Point out every Plasmodium parasite and every leukocyte.
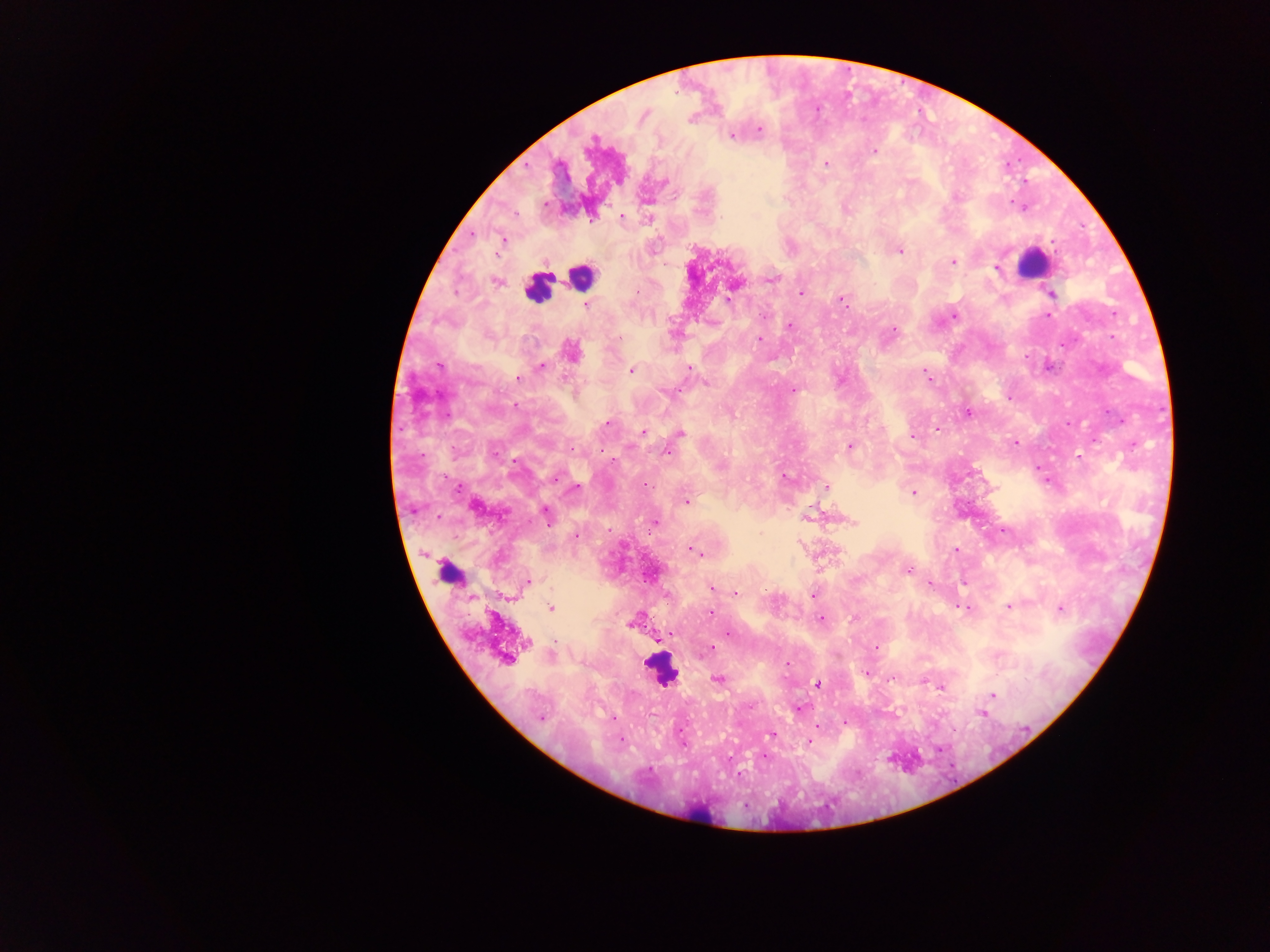

Approximate centers as {x, y} in pixels.
Plasmodium parasites: {643, 116}, {690, 119}, {759, 129}, {732, 136}, {874, 151}, {826, 164}, {664, 183}, {957, 198}, {544, 204}, {622, 216}, {721, 218}, {591, 220}, {501, 239}, {900, 251}, {954, 262}, {996, 268}, {771, 279}, {497, 281}, {637, 292}, {801, 293}, {1051, 294}, {727, 299}, {841, 300}, {586, 306}, {955, 315}, {763, 316}, {1048, 316}, {790, 326}, {893, 329}, {760, 339}, {570, 350}, {439, 366}, {542, 366}, {689, 368}, {631, 370}, {926, 372}, {519, 378}, {706, 383}, {793, 389}, {663, 391}, {967, 414}, {607, 423}, {937, 429}, {643, 432}, {680, 433}, {911, 436}, {1015, 442}, {850, 446}, {572, 448}, {667, 453}, {1078, 457}, {783, 477}, {554, 478}, {645, 485}, {577, 487}, {827, 487}, {913, 492}, {686, 502}, {477, 509}, {547, 513}, {655, 522}, {853, 522}, {761, 533}, {576, 537}, {689, 549}, {955, 550}, {696, 552}, {701, 555}, {909, 570}, {529, 580}, {931, 583}, {712, 588}, {716, 589}, {736, 592}, {812, 595}, {550, 607}, {1009, 607}, {1061, 608}, {966, 609}, {710, 612}, {854, 618}, {821, 619}, {630, 624}, {667, 634}, {729, 634}, {527, 642}, {712, 648}, {876, 648}, {505, 660}, {787, 663}, {867, 673}, {717, 679}, {818, 684}, {941, 687}, {993, 696}, {749, 706}, {981, 713}, {541, 718}, {614, 719}, {844, 723}, {816, 726}, {771, 734}, {620, 739}, {809, 742}, {763, 757}, {649, 769}.
Leukocytes: {1033, 264}, {581, 276}, {537, 288}, {448, 572}, {660, 670}, {702, 812}.

{
  "country": "Ghana",
  "capture": "mobile-phone photograph through a microscope",
  "image_size": "1270×952 pixels",
  "field_of_view": "single",
  "preparation": "thick blood smear"
}